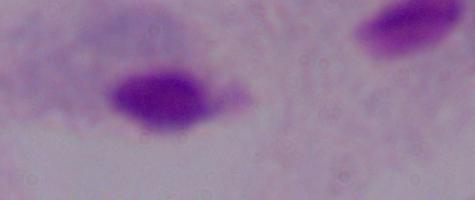
{
  "magnification": "1000x",
  "identification": "trichomonad",
  "modality": "photomicrograph"
}